Name the blood parasite species.
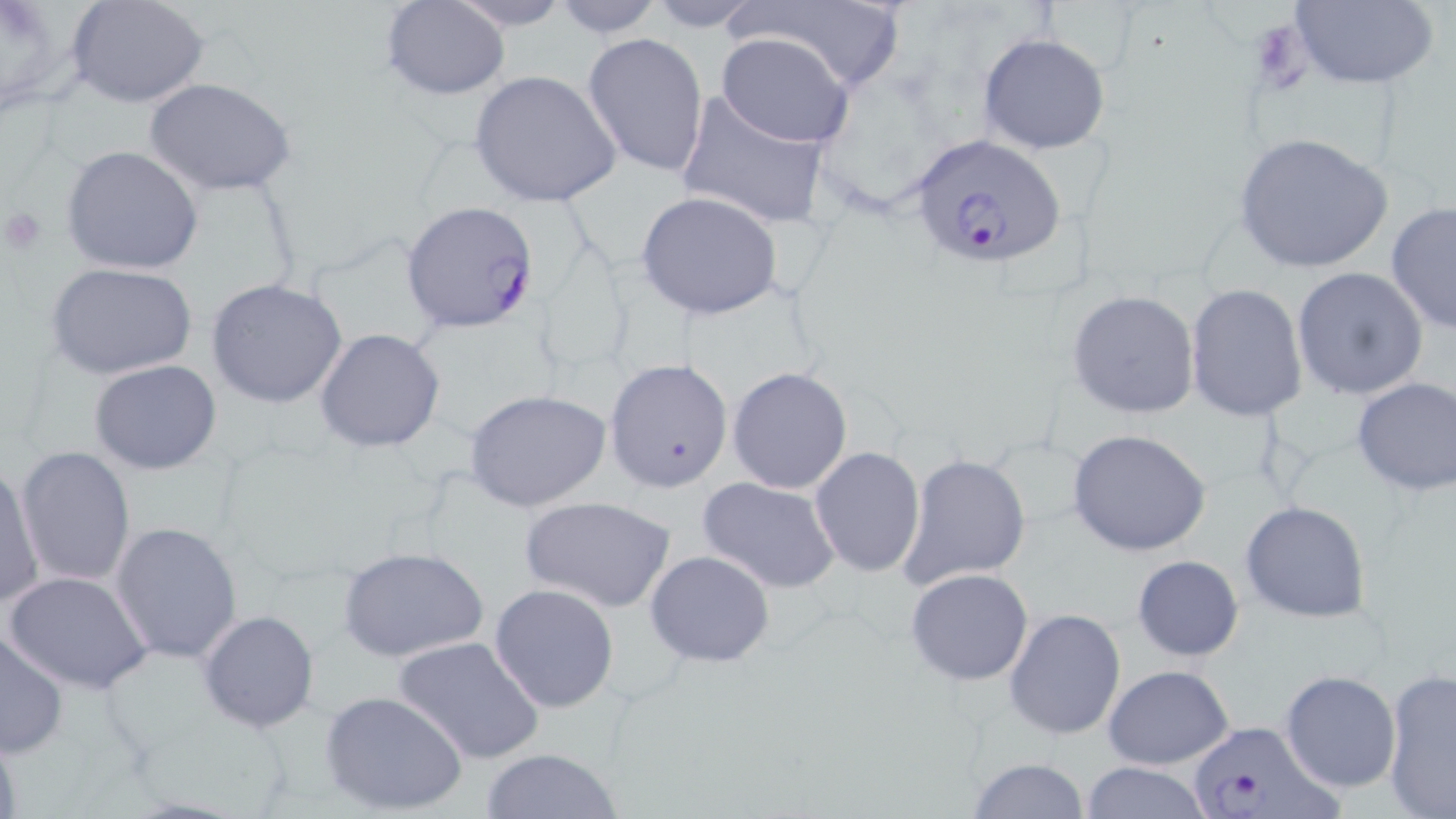

Plasmodium falciparum.

Summary:
  - Coordinate format: approximate bounding boxes as [x1, y1, x2, y2] in pixels
  - Uninfected red blood cell locations: [0, 0, 78, 119], [66, 0, 210, 108], [544, 0, 670, 38], [639, 0, 776, 30], [739, 0, 910, 95], [1286, 0, 1440, 89], [381, 1, 511, 99], [444, 1, 576, 31], [582, 32, 709, 178], [716, 33, 855, 148], [978, 33, 1109, 155], [469, 71, 622, 208], [143, 78, 296, 197], [675, 91, 830, 230], [1232, 131, 1394, 275], [60, 146, 205, 276], [636, 191, 782, 319], [1385, 201, 1456, 335], [47, 262, 197, 381], [1291, 266, 1428, 400], [205, 277, 350, 409], [1185, 284, 1309, 420], [1068, 289, 1201, 418], [315, 327, 446, 454], [603, 357, 735, 492], [90, 359, 222, 475], [727, 367, 854, 494], [1350, 377, 1456, 496], [463, 389, 612, 512], [1068, 428, 1212, 556], [15, 447, 135, 587], [807, 447, 926, 576], [899, 453, 1031, 590], [1, 458, 45, 611], [697, 475, 842, 594], [519, 496, 677, 612], [1241, 500, 1372, 623], [109, 520, 243, 663], [337, 545, 489, 663], [646, 549, 776, 669], [1131, 556, 1242, 661], [905, 567, 1033, 686], [5, 569, 154, 695], [488, 583, 619, 714], [1004, 607, 1128, 740], [197, 609, 320, 735], [1, 629, 70, 756], [392, 634, 545, 764], [1103, 664, 1235, 769], [1279, 670, 1401, 794], [1382, 670, 1456, 818], [320, 690, 466, 816], [0, 724, 22, 819], [478, 746, 625, 819], [967, 758, 1092, 817], [1079, 761, 1212, 819]
  - Plasmodium falciparum-infected red blood cell locations: [909, 131, 1066, 269], [402, 201, 541, 334], [1186, 720, 1337, 819]
  - Platelet locations: [2, 205, 47, 254]
  - Modality: optical microscopy
  - Field of view: single
  - Stain: May-Grünwald-Giemsa
  - Magnification: 1000x
  - Preparation: thin blood smear
  - Image size: 1456×819 pixels